Mark where cells are.
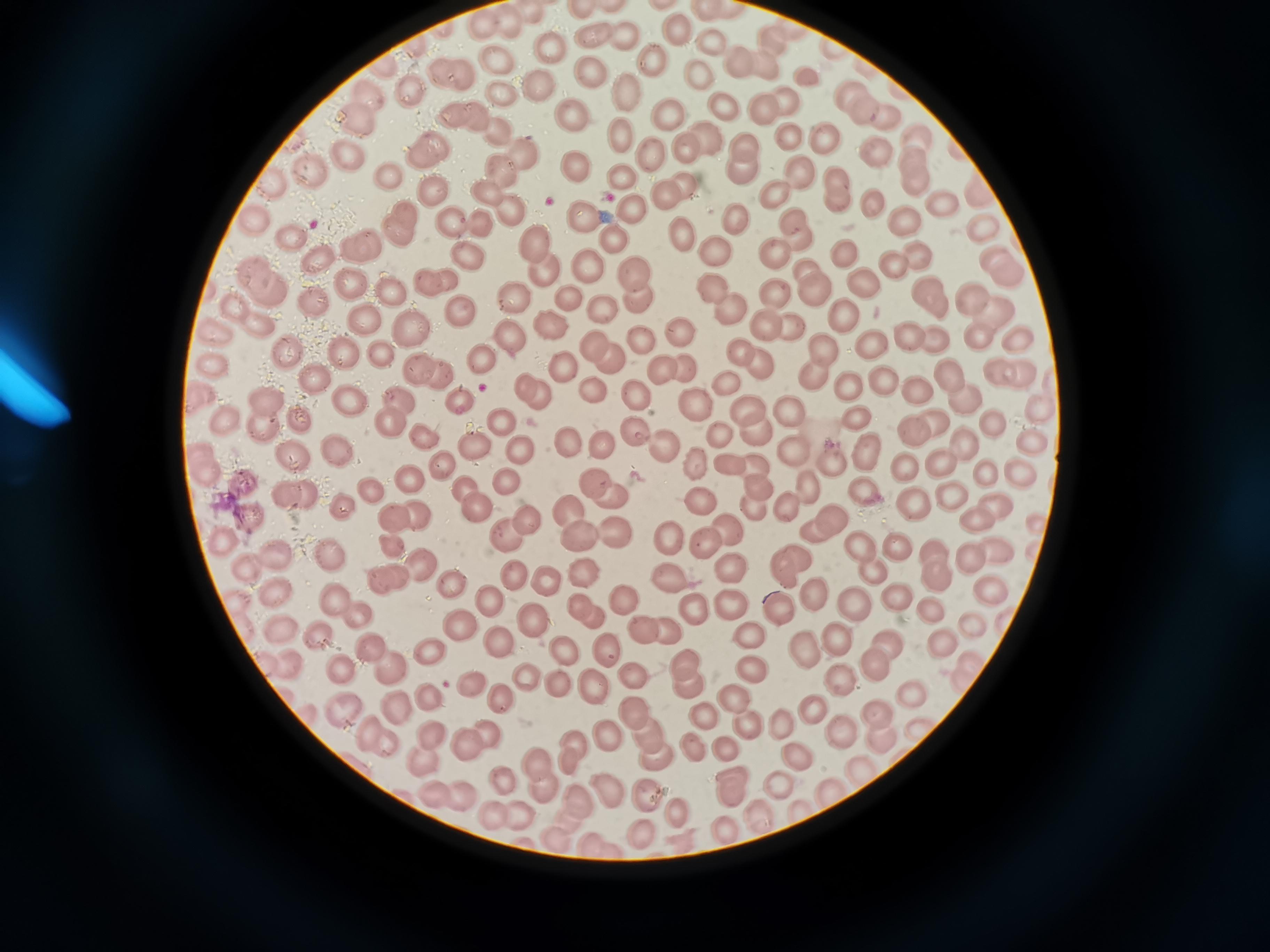

Approximate centers as [x, y] in pixels.
Cells: [580, 10], [507, 20], [475, 21], [679, 24], [593, 36], [621, 36], [774, 39], [708, 41], [553, 44], [411, 46], [495, 60], [647, 60], [739, 61], [761, 61], [383, 62], [442, 72], [587, 73], [459, 74], [808, 74], [700, 80], [534, 81], [408, 90], [848, 91], [366, 94], [625, 94], [505, 97], [785, 98], [763, 107], [723, 109], [862, 109], [572, 110], [887, 114], [451, 116], [470, 116], [667, 119], [353, 121], [495, 128], [622, 133], [822, 135], [789, 137], [918, 137], [745, 143], [689, 148], [521, 150], [427, 151], [650, 151], [876, 151], [344, 153], [912, 156], [579, 161], [499, 168], [305, 170], [797, 170], [385, 171], [739, 173], [620, 175], [837, 175], [269, 177], [685, 180], [914, 180], [485, 185], [434, 187], [669, 193], [778, 193], [838, 199], [869, 199], [943, 200], [629, 202], [506, 207], [581, 216], [734, 216], [901, 216], [792, 218], [250, 219], [484, 222], [448, 223], [400, 225], [984, 227], [680, 229], [290, 235], [613, 237], [795, 239], [537, 244], [363, 245], [713, 247], [916, 251], [768, 253], [842, 253], [470, 254], [996, 256], [319, 257], [586, 265], [894, 266], [542, 267], [635, 269], [810, 271], [1012, 272], [347, 275], [860, 278], [264, 279], [435, 279], [710, 288], [640, 290], [773, 290], [389, 291], [815, 293], [515, 295], [967, 296], [571, 299], [931, 299], [311, 300], [727, 303], [601, 308], [998, 311], [249, 312], [462, 313], [845, 314], [365, 322], [412, 322], [548, 322], [790, 325], [760, 330], [680, 331], [910, 332], [508, 335], [977, 335], [644, 338], [1019, 339], [934, 342], [593, 343], [867, 348], [284, 349], [744, 351], [824, 351], [382, 352], [610, 355], [481, 360], [759, 363], [213, 365], [416, 365], [564, 365], [662, 368], [684, 368], [440, 371], [996, 372], [312, 373], [1020, 373], [811, 374], [947, 377], [876, 378], [724, 385], [848, 387], [592, 388], [534, 390], [917, 391], [197, 395], [634, 397], [265, 398], [397, 398], [961, 398], [348, 399], [461, 402], [747, 403], [693, 406], [788, 409], [1041, 409], [223, 414], [298, 414], [991, 419], [389, 422], [854, 422], [937, 422], [502, 424], [261, 426], [753, 431], [917, 431], [717, 433], [631, 435], [423, 438], [1031, 439], [963, 440], [598, 441], [471, 443], [567, 443], [661, 444], [198, 447], [789, 447], [334, 449], [519, 449], [861, 450], [944, 462], [442, 463], [698, 463], [837, 463], [728, 465], [907, 466], [752, 467], [206, 468], [1020, 471], [984, 473], [241, 480], [412, 480], [505, 483], [594, 484], [806, 484], [861, 488], [460, 489], [761, 490], [949, 493], [372, 494], [908, 495], [295, 496], [607, 496], [702, 502], [478, 507], [789, 507], [997, 509], [571, 510], [751, 510], [416, 513], [247, 515], [824, 515], [393, 516], [974, 520], [528, 521], [1037, 525], [724, 530], [814, 531], [615, 532], [665, 533], [578, 534], [219, 537], [506, 538], [698, 539], [390, 541], [863, 544], [893, 546], [989, 549], [935, 550], [273, 553], [329, 554], [971, 556], [416, 566], [730, 567], [786, 567], [246, 568], [868, 569], [517, 570], [585, 570], [934, 572], [389, 576], [543, 576], [667, 578], [450, 582], [277, 592], [813, 592], [989, 592], [333, 593], [620, 594], [898, 597], [488, 598], [731, 601], [848, 603], [582, 605], [777, 608], [931, 608], [353, 613], [593, 613], [690, 613], [534, 616], [455, 624], [970, 624], [661, 627], [280, 629], [642, 630], [744, 630], [321, 637], [838, 639], [497, 640], [943, 641], [887, 643], [564, 647], [370, 648], [606, 648], [803, 651], [426, 653], [969, 660], [684, 661], [285, 663], [875, 664], [384, 665], [751, 666], [341, 671], [526, 676], [632, 677], [837, 677], [957, 680], [470, 681], [691, 682], [560, 683], [590, 687], [912, 693], [425, 695], [503, 697], [732, 701], [395, 706], [337, 707], [810, 710], [632, 711], [701, 715], [877, 716], [780, 721], [744, 728], [430, 731], [843, 733], [375, 734], [485, 734], [647, 734], [608, 737], [878, 739], [462, 741], [573, 743], [691, 746], [719, 746], [796, 755], [656, 758], [424, 759], [569, 760], [539, 762], [862, 773], [498, 776], [730, 785], [774, 786], [538, 787], [602, 787], [426, 790], [827, 793], [645, 794], [463, 796], [578, 799], [801, 805], [759, 811], [490, 812], [676, 815], [522, 816], [719, 825], [640, 832], [556, 835], [600, 844].

Image is 1270×952 pixels. One field from this slide. Acquired by smartphone through the microscope eyepiece. Giemsa-stained preparation. Thin blood smear.